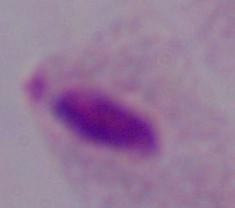

1000x magnification. Micrograph. A trichomonad is shown.